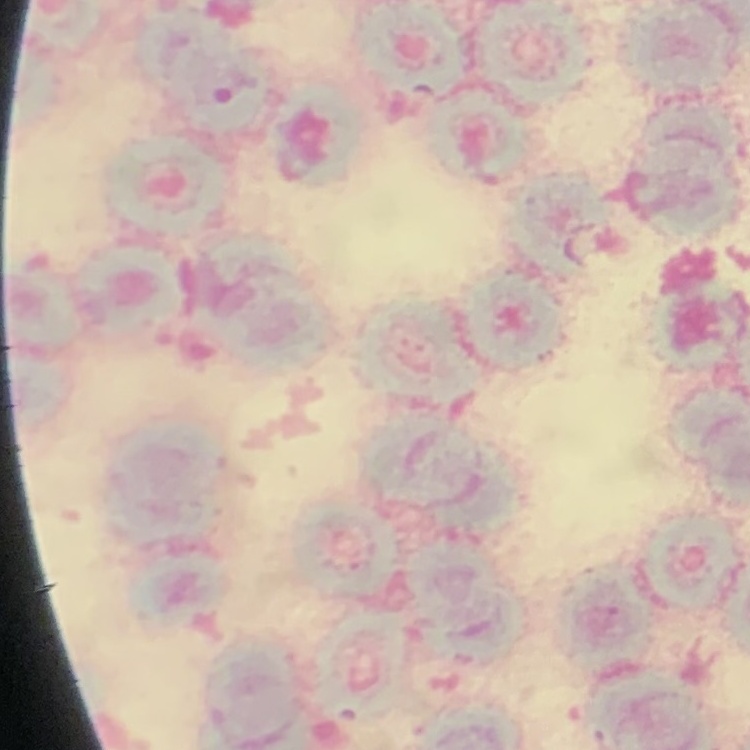
Summary:
  - Erythrocyte morphology: rouleaux formation
  - Stain: Field's or Giemsa
  - Preparation: thin blood smear
  - Image type: square crop of a larger photomicrograph